Outline each blood parasite and name the species.
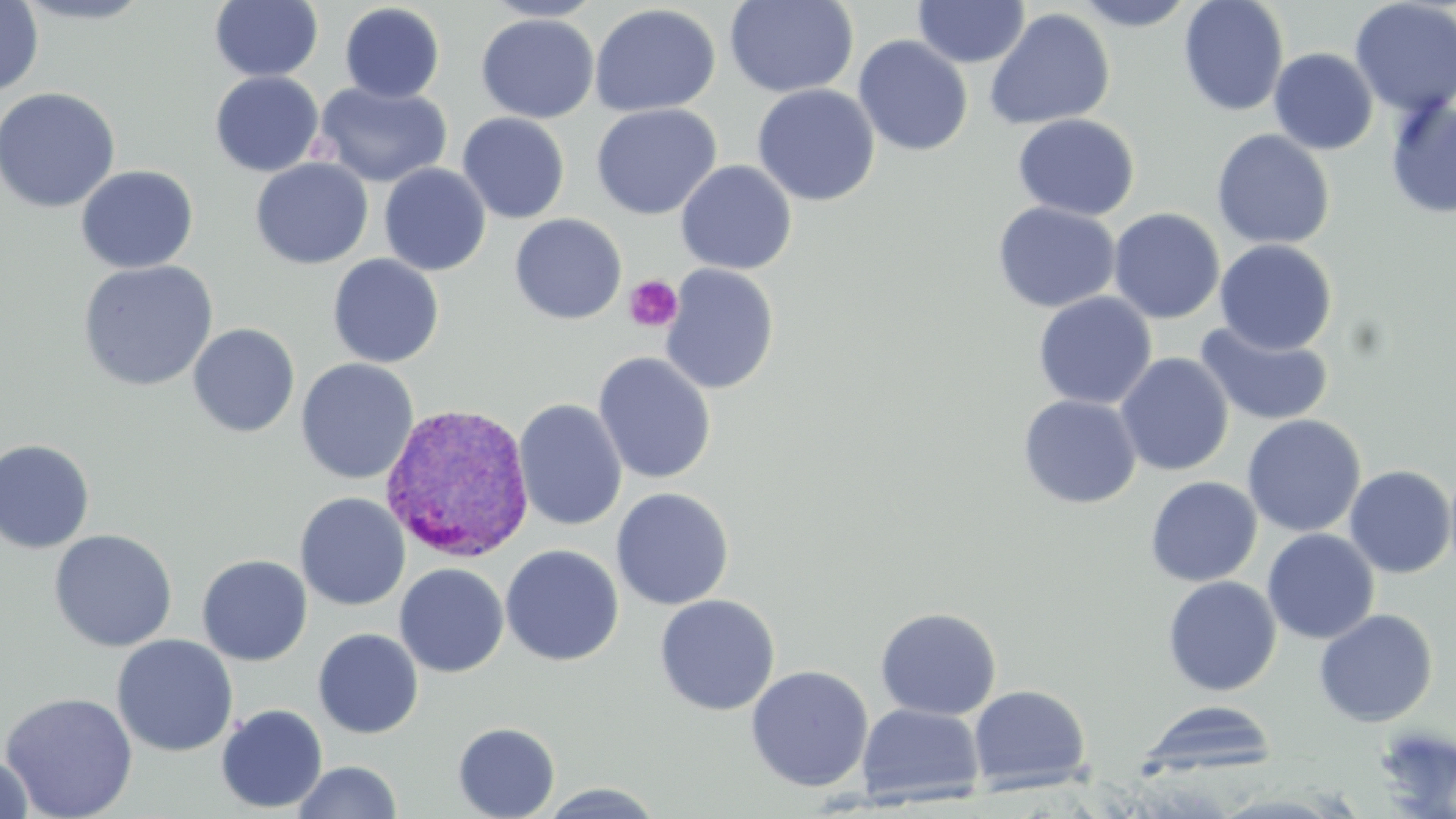

Approximate bounding boxes as (x1, y1, x2, y2) in pixels.
Plasmodium vivax-infected red blood cells: (380, 401, 537, 564).
No Plasmodium falciparum, Plasmodium ovale, Plasmodium malariae, Babesia divergens, or Trypanosoma brucei observed.

slide-level diagnosis = Plasmodium vivax
modality = optical microscopy
magnification = 1000x
stain = May-Grünwald-Giemsa
platelet locations = approximate bounding boxes as (x1, y1, x2, y2) in pixels: (623, 274, 683, 333)
preparation = thin blood smear
uninfected red blood cell locations = approximate bounding boxes as (x1, y1, x2, y2) in pixels: (9, 0, 156, 25), (209, 0, 325, 83), (480, 0, 607, 22), (724, 0, 858, 98), (912, 0, 1030, 69), (1071, 0, 1199, 31), (1178, 0, 1290, 116), (1349, 0, 1456, 117), (0, 1, 43, 98), (339, 3, 446, 103), (589, 3, 721, 117), (984, 7, 1116, 131), (476, 13, 599, 123), (853, 35, 974, 156), (1269, 48, 1378, 155), (209, 71, 323, 177), (314, 82, 451, 188), (752, 84, 880, 206), (0, 87, 121, 213), (1384, 95, 1456, 220), (591, 103, 722, 220), (457, 112, 570, 224), (1012, 113, 1139, 221), (1211, 129, 1335, 250), (250, 158, 373, 269), (675, 160, 797, 274), (378, 163, 490, 276), (76, 165, 199, 273), (992, 201, 1121, 313), (1108, 207, 1225, 323), (509, 213, 627, 325), (1214, 239, 1337, 355), (328, 254, 445, 368), (77, 259, 218, 392), (660, 264, 780, 395), (1033, 291, 1157, 410), (1194, 321, 1335, 427), (187, 323, 300, 437), (593, 352, 717, 484), (1115, 352, 1234, 476), (296, 358, 418, 485), (1017, 394, 1142, 509), (514, 398, 628, 532), (1242, 414, 1366, 537), (0, 439, 95, 554), (1343, 465, 1456, 578), (1145, 476, 1262, 587), (611, 487, 734, 610), (295, 492, 410, 611), (1262, 528, 1380, 645), (49, 529, 177, 652), (500, 544, 624, 666), (196, 554, 312, 666), (394, 563, 509, 677), (1162, 575, 1282, 697), (655, 594, 780, 716), (875, 607, 1002, 720), (1314, 608, 1438, 727), (313, 628, 424, 739), (112, 634, 238, 756), (745, 665, 874, 792), (968, 684, 1091, 793), (0, 692, 138, 819), (1135, 700, 1278, 779), (857, 703, 984, 805), (216, 705, 328, 813), (453, 722, 560, 819), (1372, 727, 1456, 812), (0, 754, 34, 818), (292, 760, 403, 818), (536, 783, 667, 818)
image size = 1456×819 pixels
field of view = one of a larger specimen